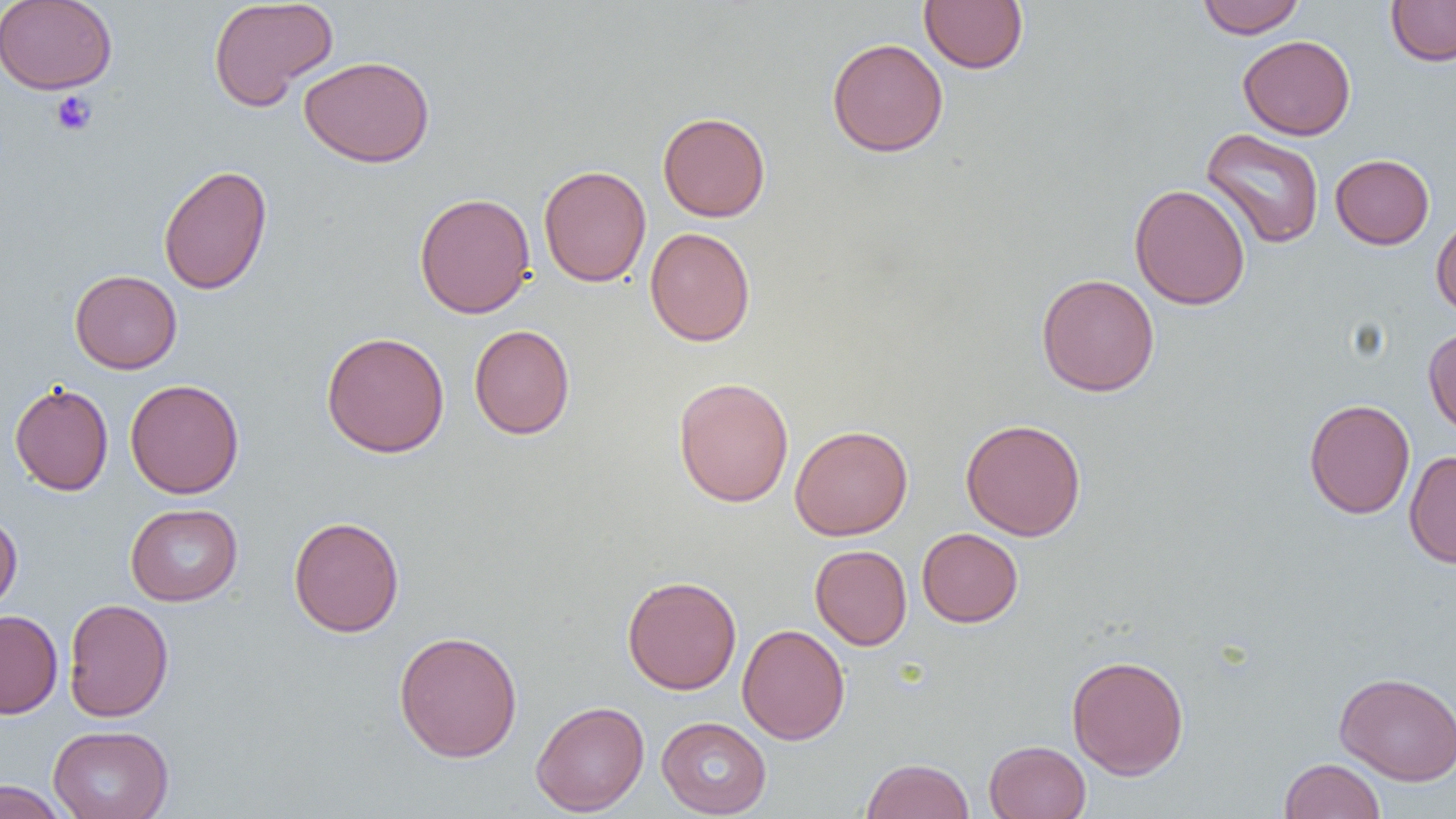
Summary:
  - Coordinate format: approximate bounding boxes as named x1/y1/x2/y2 corners in pixels
  - Uninfected red blood cell locations: (x1=0, y1=0, x2=117, y2=94), (x1=208, y1=0, x2=338, y2=110), (x1=919, y1=0, x2=1028, y2=74), (x1=1196, y1=0, x2=1306, y2=38), (x1=1386, y1=0, x2=1456, y2=66), (x1=1238, y1=35, x2=1356, y2=140), (x1=827, y1=38, x2=949, y2=157), (x1=299, y1=54, x2=435, y2=168), (x1=657, y1=111, x2=771, y2=222), (x1=1201, y1=127, x2=1325, y2=249), (x1=1330, y1=154, x2=1434, y2=249), (x1=157, y1=164, x2=273, y2=295), (x1=538, y1=165, x2=652, y2=287), (x1=1129, y1=183, x2=1251, y2=310), (x1=414, y1=191, x2=536, y2=319), (x1=1431, y1=214, x2=1456, y2=319), (x1=644, y1=226, x2=756, y2=346), (x1=69, y1=270, x2=182, y2=374), (x1=1036, y1=273, x2=1160, y2=397), (x1=469, y1=324, x2=575, y2=439), (x1=1423, y1=327, x2=1456, y2=436), (x1=321, y1=331, x2=450, y2=458), (x1=673, y1=376, x2=794, y2=507), (x1=125, y1=379, x2=244, y2=498), (x1=9, y1=382, x2=114, y2=496), (x1=1304, y1=398, x2=1415, y2=518), (x1=960, y1=419, x2=1086, y2=541), (x1=789, y1=424, x2=913, y2=540), (x1=1404, y1=450, x2=1456, y2=569), (x1=126, y1=503, x2=243, y2=606), (x1=0, y1=512, x2=22, y2=613), (x1=288, y1=515, x2=404, y2=637), (x1=917, y1=528, x2=1023, y2=627), (x1=810, y1=544, x2=912, y2=650), (x1=622, y1=575, x2=741, y2=695), (x1=63, y1=597, x2=174, y2=722), (x1=0, y1=610, x2=63, y2=718), (x1=736, y1=623, x2=850, y2=745), (x1=393, y1=630, x2=523, y2=762), (x1=1066, y1=654, x2=1190, y2=779), (x1=1334, y1=671, x2=1456, y2=786), (x1=530, y1=700, x2=650, y2=816), (x1=656, y1=716, x2=772, y2=818), (x1=47, y1=724, x2=174, y2=819), (x1=984, y1=740, x2=1091, y2=818), (x1=860, y1=757, x2=975, y2=819), (x1=1279, y1=758, x2=1386, y2=819), (x1=0, y1=780, x2=71, y2=818)
  - Platelet locations: (x1=49, y1=90, x2=98, y2=136)
  - Slide-level diagnosis: negative for blood parasites
  - Image size: 1456×819 pixels
  - Magnification: 1000x
  - Modality: optical microscopy
  - Field of view: one of a larger specimen
  - Preparation: thin blood film